Locate every blood parasite and identify its species.
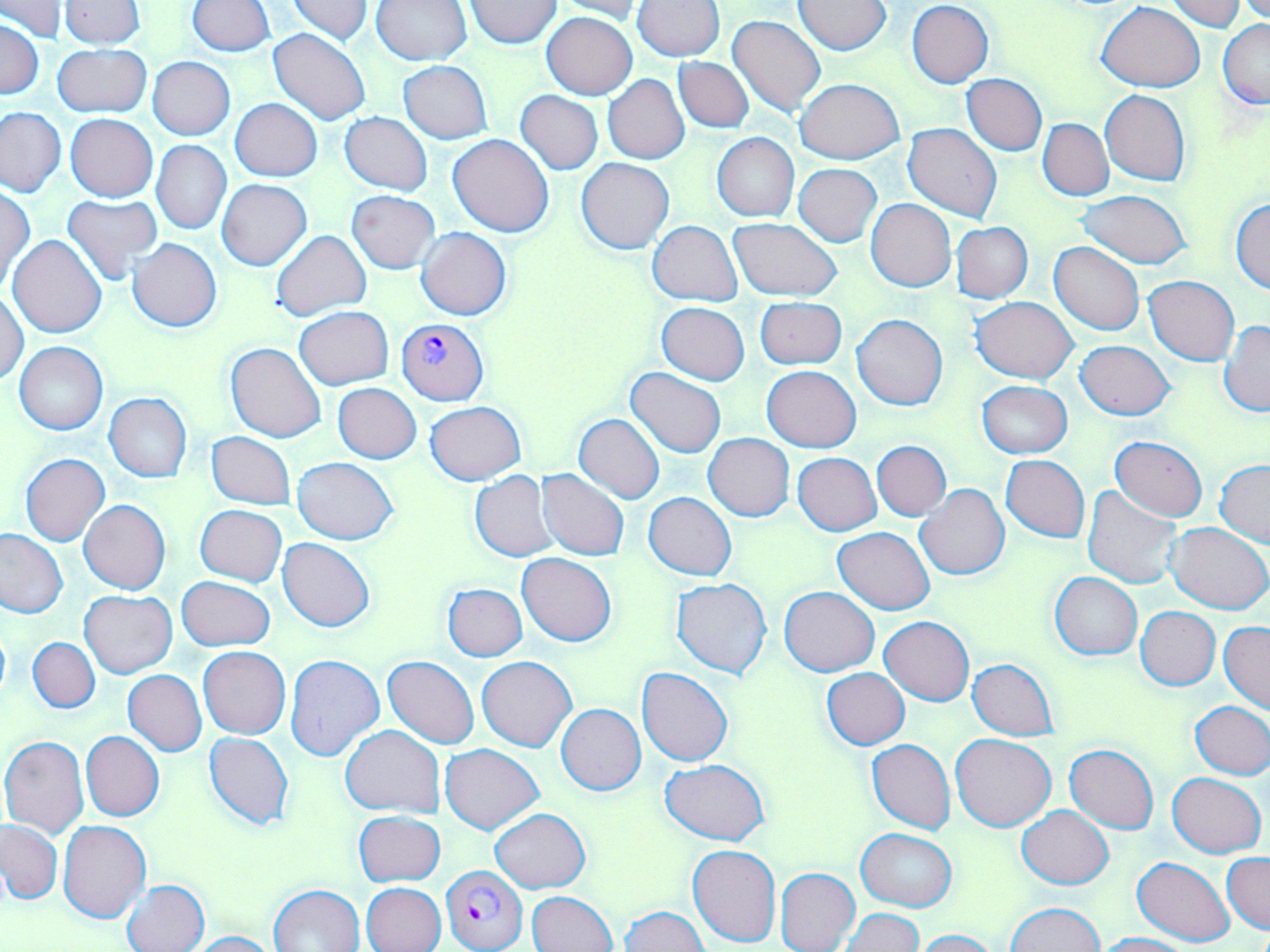

Approximate bounding boxes as (x1, y1, x2, y2) in pixels.
Plasmodium falciparum-infected red blood cells: (395, 317, 488, 406), (441, 865, 528, 952).
No Plasmodium ovale, Plasmodium malariae, Plasmodium vivax, Babesia divergens, or Trypanosoma brucei observed.

Summary:
  - Uninfected red blood cell locations: (2, 0, 66, 40), (286, 0, 374, 45), (547, 0, 648, 19), (1238, 0, 1270, 22), (58, 1, 147, 50), (188, 1, 275, 55), (370, 1, 473, 67), (465, 1, 561, 48), (634, 1, 724, 60), (794, 1, 893, 55), (907, 1, 994, 88), (1165, 1, 1249, 33), (1096, 2, 1205, 91), (542, 12, 637, 100), (727, 14, 825, 119), (0, 18, 44, 100), (1218, 20, 1270, 110), (269, 28, 371, 126), (52, 42, 151, 119), (674, 56, 754, 132), (148, 57, 234, 140), (398, 60, 493, 143), (962, 73, 1046, 156), (603, 75, 689, 164), (795, 78, 905, 164), (515, 90, 603, 174), (1101, 90, 1191, 186), (229, 98, 321, 181), (0, 107, 66, 197), (340, 112, 432, 195), (65, 114, 158, 202), (1038, 118, 1113, 200), (903, 122, 1002, 223), (712, 133, 799, 222), (449, 134, 554, 238), (152, 140, 231, 234), (576, 157, 674, 254), (794, 164, 882, 247), (216, 179, 312, 271), (1, 186, 34, 290), (347, 189, 439, 273), (1075, 189, 1192, 270), (62, 193, 161, 286), (866, 198, 956, 292), (1232, 199, 1270, 294), (727, 218, 842, 302), (648, 220, 742, 305), (951, 221, 1034, 303), (417, 228, 511, 321), (272, 229, 370, 323), (8, 235, 107, 340), (127, 238, 222, 332), (1049, 242, 1144, 335), (1144, 276, 1239, 365), (1, 290, 28, 386), (755, 297, 846, 370), (971, 297, 1077, 383), (656, 302, 749, 385), (294, 306, 394, 389), (852, 315, 948, 410), (1219, 321, 1270, 416), (15, 341, 108, 435), (1076, 341, 1174, 420), (226, 342, 328, 443), (762, 366, 860, 452), (626, 368, 726, 457), (977, 380, 1073, 459), (332, 384, 422, 464), (103, 393, 192, 482), (425, 401, 524, 484), (574, 413, 664, 503), (206, 432, 296, 510), (704, 433, 794, 521), (1110, 435, 1207, 520), (872, 440, 951, 521), (21, 453, 110, 547), (793, 453, 881, 535), (1001, 455, 1089, 543), (292, 457, 397, 544), (1215, 461, 1270, 545), (536, 469, 630, 561), (470, 471, 560, 562), (915, 484, 1009, 581), (1081, 486, 1184, 588), (643, 492, 736, 580), (79, 499, 171, 594), (195, 505, 287, 585), (1166, 523, 1270, 612), (833, 527, 935, 613), (0, 528, 68, 619), (277, 538, 375, 631), (517, 553, 616, 645), (1050, 571, 1142, 661), (177, 576, 275, 652), (672, 577, 772, 679), (443, 584, 527, 661), (780, 586, 879, 676), (80, 591, 176, 678), (1136, 606, 1220, 690), (880, 616, 974, 705), (1219, 621, 1270, 714), (0, 623, 10, 706), (28, 637, 99, 713), (199, 647, 290, 739), (285, 654, 386, 762), (383, 656, 479, 749), (477, 656, 577, 751), (967, 659, 1059, 740), (636, 667, 733, 766), (822, 668, 909, 750), (123, 670, 207, 756), (1191, 700, 1269, 780), (555, 704, 646, 795), (340, 724, 445, 818), (81, 731, 164, 822), (205, 733, 294, 829), (951, 734, 1056, 832), (1, 735, 89, 838), (865, 738, 956, 834), (441, 744, 543, 834), (1065, 745, 1159, 833), (661, 760, 770, 844), (1167, 772, 1266, 858), (1018, 806, 1114, 888), (490, 809, 590, 893), (354, 811, 445, 886), (0, 819, 62, 904), (58, 820, 150, 922), (856, 829, 956, 912), (687, 843, 782, 946), (1223, 852, 1269, 934), (1131, 855, 1236, 945), (775, 867, 860, 952), (122, 879, 210, 952), (360, 883, 445, 952), (268, 884, 364, 952), (527, 891, 618, 952), (1007, 902, 1103, 952), (620, 906, 708, 952), (839, 908, 923, 950), (912, 928, 999, 952), (186, 931, 279, 952), (1096, 933, 1194, 952)
  - Slide-level diagnosis: Plasmodium falciparum
  - Magnification: 1000x
  - Modality: optical microscopy
  - Image size: 1270×952 pixels
  - Field of view: one of a larger specimen
  - Preparation: thin blood smear
  - Stain: May-Grünwald-Giemsa